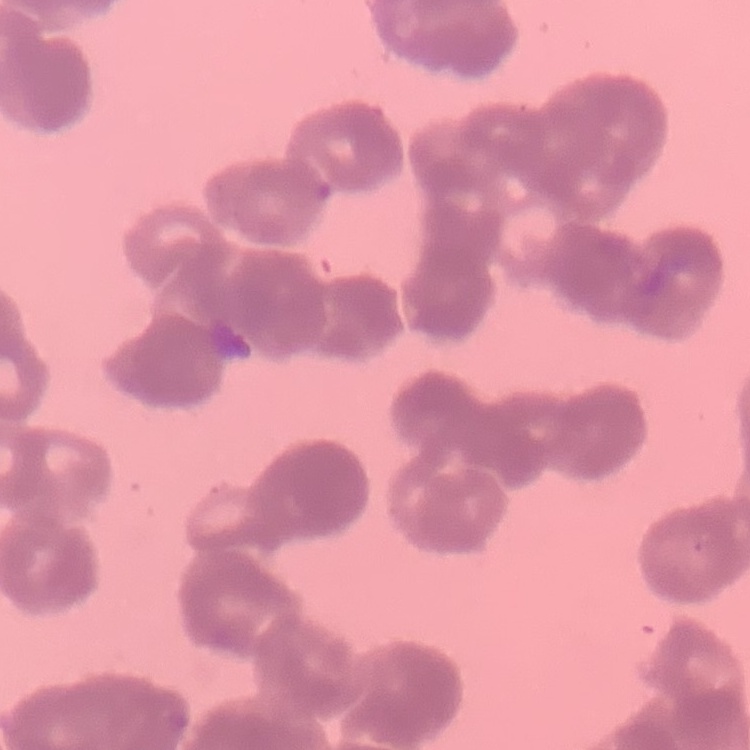

The erythrocytes exhibit rouleaux formation. Square crop of a larger photomicrograph. Stained with either Field's or Giemsa. Thin peripheral smear.